Classify this cell by malaria status.
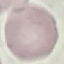

Uninfected.

Summary:
  - Image type: cell patch, automatically extracted from a larger field of view and resized to 64 × 64 pixels
  - Capture: smartphone through the microscope eyepiece
  - Stain: Giemsa
  - Preparation: thin smear